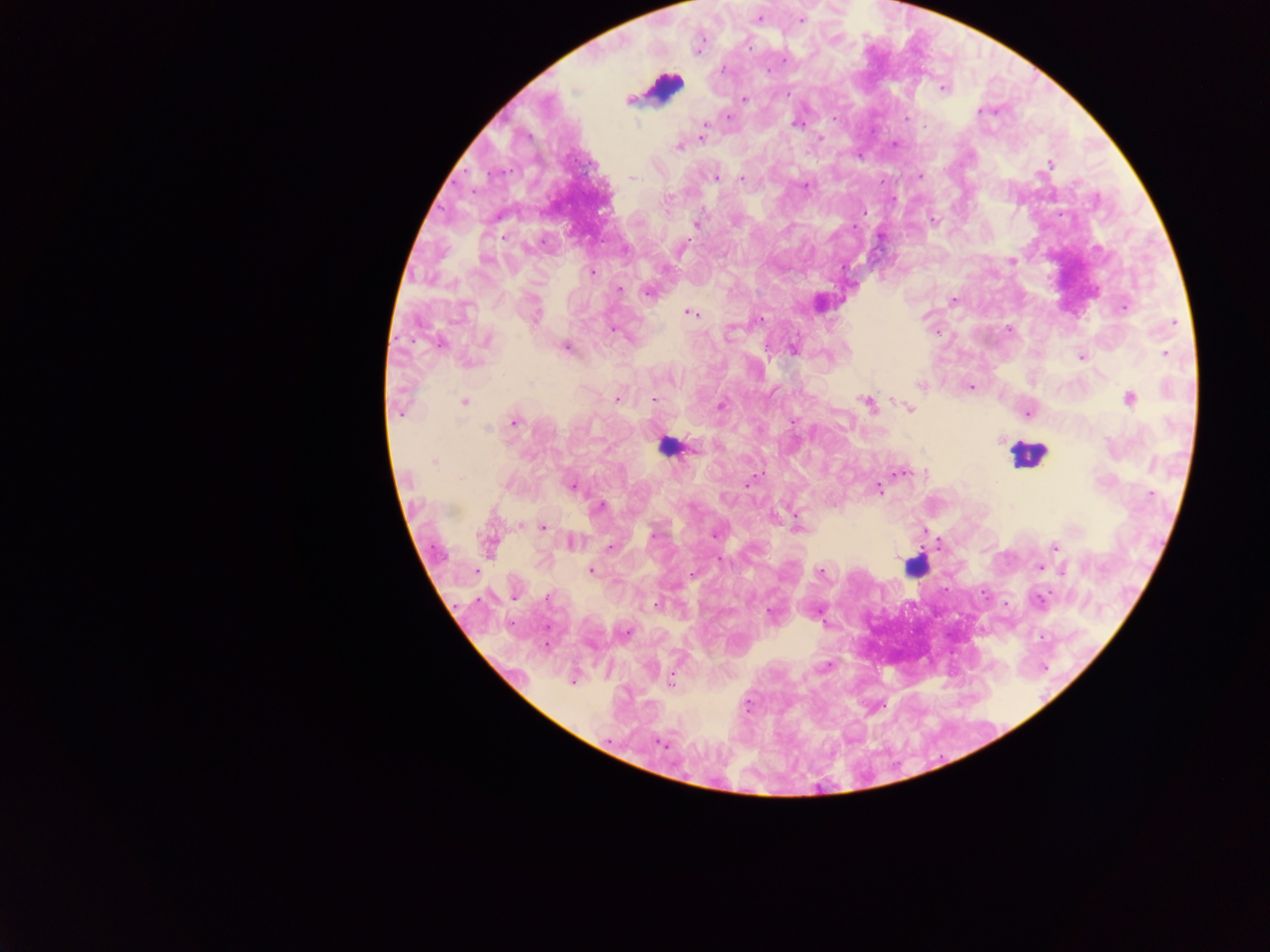
Approximate centers as (x, y) in pixels. Leukocyte locations: (665, 86), (667, 447), (1027, 453), (914, 567). Plasmodium parasite locations: (759, 19), (801, 21), (749, 48), (785, 61), (722, 70), (767, 70), (942, 88), (628, 99), (744, 99), (980, 111), (728, 116), (834, 118), (907, 118), (796, 124), (705, 126), (701, 137), (820, 137), (895, 144), (678, 147), (1049, 165), (920, 177), (632, 178), (715, 178), (742, 179), (805, 186), (668, 199), (864, 212), (934, 220), (696, 223), (504, 237), (681, 248), (1012, 262), (592, 272), (619, 289), (648, 293), (954, 300), (1124, 308), (691, 313), (535, 316), (761, 319), (1173, 323), (1008, 329), (613, 330), (487, 340), (440, 344), (565, 348), (793, 349), (1165, 354), (1081, 357), (920, 385), (971, 387), (617, 399), (1130, 399), (654, 400), (464, 403), (866, 403), (721, 405), (908, 409), (400, 411), (1027, 414), (514, 421), (794, 421), (487, 429), (695, 449), (433, 461), (900, 472), (747, 484), (571, 485), (878, 489), (600, 506), (797, 525), (544, 527), (653, 535), (714, 535), (571, 543), (489, 545), (1055, 546), (610, 547), (1040, 568), (590, 571), (1064, 571), (476, 572), (820, 573), (514, 597), (547, 598), (1039, 600), (656, 604), (771, 612), (627, 633), (546, 645), (827, 665), (671, 681), (572, 682), (661, 744). Thick blood smear. Sample from Ghana. Photographed through a microscope with a mobile-phone camera. Image is 1270×952 pixels. One field of view.